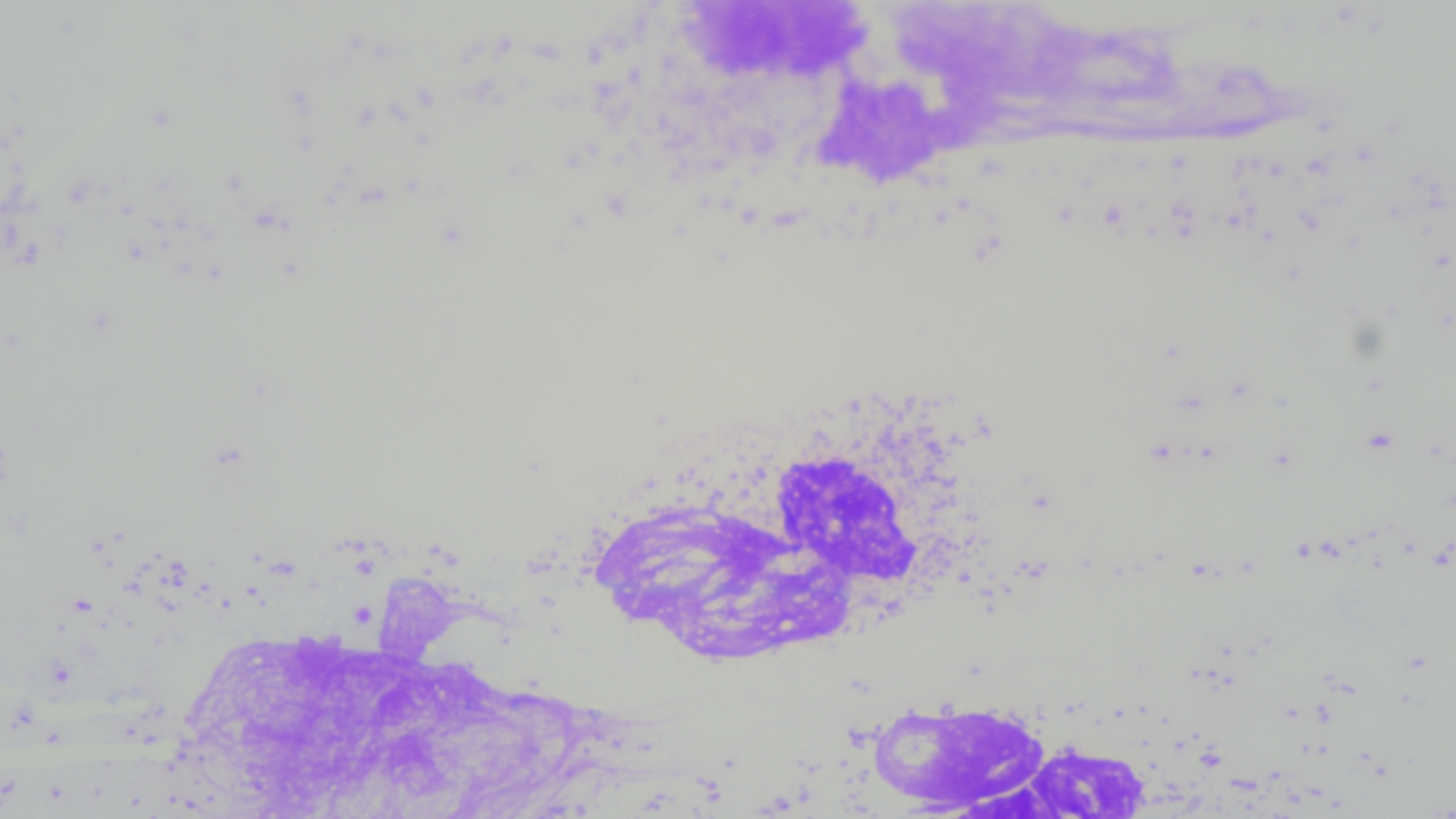
Summary:
  - Coordinate format: approximate bounding boxes as (x1, y1, x2, y2) in pixels
  - White blood cell locations: (660, 2, 1380, 262), (660, 377, 993, 659), (166, 577, 665, 819), (874, 697, 1167, 818)
  - Slide-level diagnosis: negative for blood parasites
  - Magnification: 1000x
  - Preparation: thin blood film
  - Field of view: single
  - Image size: 1456×819 pixels
  - Modality: optical microscopy